Assess this cell for malaria.
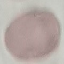
Uninfected.

{
  "stain": "Giemsa",
  "preparation": "thin smear",
  "capture": "smartphone through the microscope eyepiece",
  "image_type": "automatically extracted cell patch, resized to 64 × 64 pixels"
}